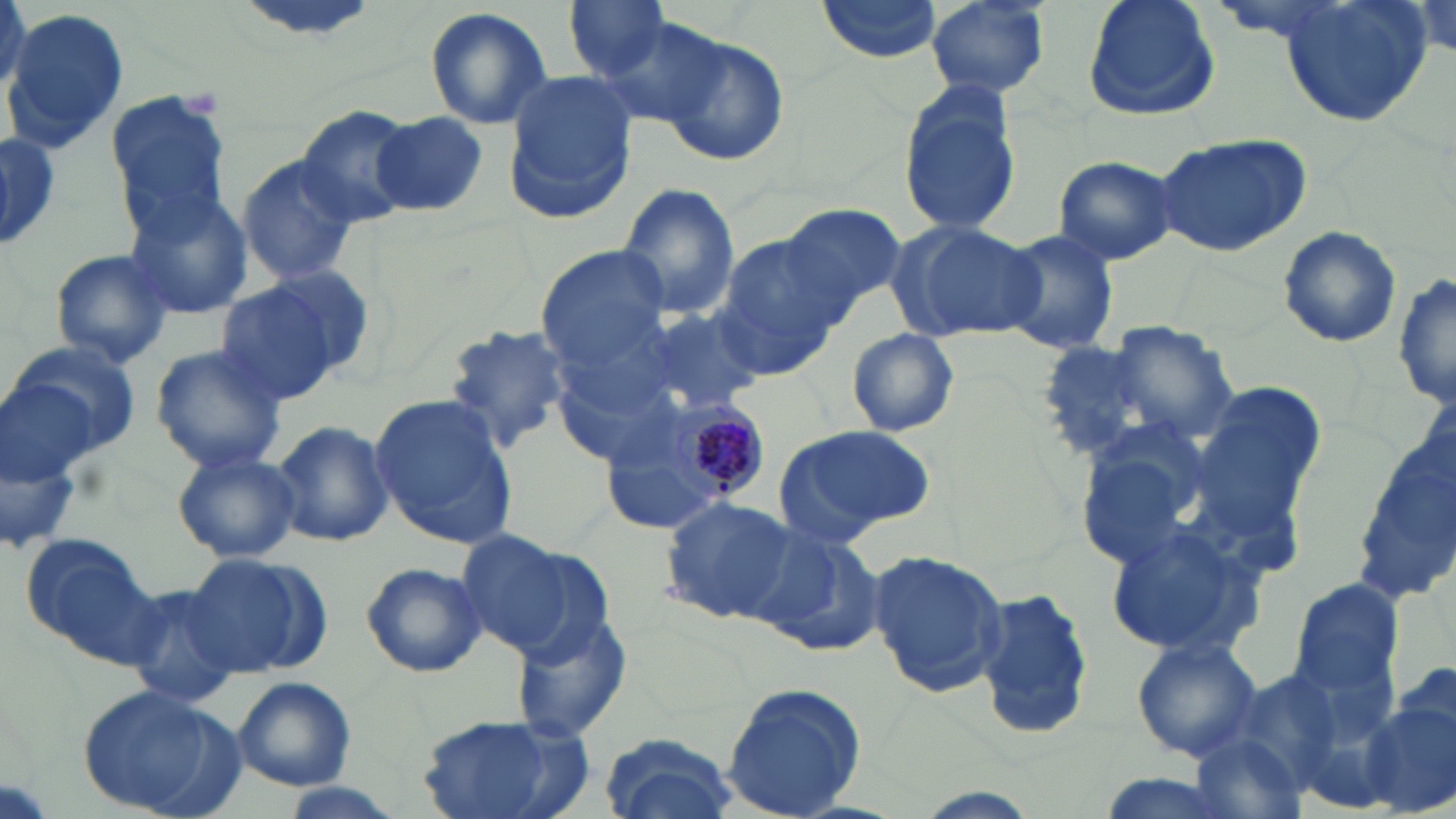

Approximate bounding boxes as named x1/y1/x2/y2 corners in pixels. Uninfected red blood cell locations: (x1=0, y1=0, x2=30, y2=98), (x1=815, y1=0, x2=950, y2=64), (x1=923, y1=0, x2=1052, y2=100), (x1=1083, y1=0, x2=1220, y2=123), (x1=1270, y1=0, x2=1434, y2=127), (x1=1411, y1=1, x2=1455, y2=54), (x1=564, y1=2, x2=674, y2=80), (x1=424, y1=6, x2=554, y2=132), (x1=3, y1=10, x2=128, y2=156), (x1=589, y1=17, x2=734, y2=128), (x1=654, y1=34, x2=787, y2=166), (x1=504, y1=73, x2=638, y2=221), (x1=898, y1=80, x2=1025, y2=239), (x1=104, y1=93, x2=234, y2=233), (x1=294, y1=105, x2=415, y2=223), (x1=375, y1=113, x2=488, y2=217), (x1=1154, y1=131, x2=1312, y2=258), (x1=0, y1=134, x2=61, y2=252), (x1=237, y1=154, x2=361, y2=286), (x1=1051, y1=155, x2=1179, y2=265), (x1=618, y1=184, x2=741, y2=322), (x1=120, y1=189, x2=255, y2=320), (x1=778, y1=203, x2=906, y2=313), (x1=889, y1=218, x2=1047, y2=343), (x1=1277, y1=224, x2=1404, y2=350), (x1=993, y1=229, x2=1123, y2=356), (x1=710, y1=236, x2=848, y2=379), (x1=539, y1=247, x2=669, y2=368), (x1=46, y1=248, x2=175, y2=369), (x1=260, y1=267, x2=379, y2=385), (x1=1394, y1=270, x2=1455, y2=412), (x1=214, y1=279, x2=348, y2=405), (x1=629, y1=307, x2=769, y2=420), (x1=441, y1=322, x2=578, y2=455), (x1=1103, y1=323, x2=1239, y2=445), (x1=846, y1=328, x2=960, y2=437), (x1=10, y1=338, x2=145, y2=461), (x1=1036, y1=342, x2=1170, y2=463), (x1=151, y1=345, x2=290, y2=473), (x1=1195, y1=382, x2=1327, y2=527), (x1=367, y1=393, x2=520, y2=547), (x1=1354, y1=412, x2=1455, y2=613), (x1=273, y1=418, x2=394, y2=547), (x1=774, y1=425, x2=935, y2=543), (x1=171, y1=450, x2=301, y2=564), (x1=658, y1=494, x2=799, y2=621), (x1=1100, y1=522, x2=1270, y2=662), (x1=746, y1=525, x2=884, y2=658), (x1=456, y1=528, x2=601, y2=657), (x1=20, y1=533, x2=163, y2=666), (x1=868, y1=550, x2=1011, y2=696), (x1=181, y1=552, x2=331, y2=678), (x1=360, y1=561, x2=488, y2=678), (x1=1286, y1=578, x2=1409, y2=708), (x1=120, y1=583, x2=245, y2=710), (x1=975, y1=584, x2=1092, y2=741), (x1=511, y1=609, x2=636, y2=744), (x1=1131, y1=636, x2=1263, y2=763), (x1=232, y1=676, x2=356, y2=790), (x1=720, y1=681, x2=867, y2=817), (x1=76, y1=684, x2=240, y2=819), (x1=1358, y1=686, x2=1456, y2=816), (x1=411, y1=715, x2=595, y2=819), (x1=597, y1=730, x2=736, y2=819), (x1=1188, y1=731, x2=1309, y2=819). Plasmodium malariae-infected red blood cell locations: (x1=663, y1=396, x2=769, y2=502). Platelet locations: (x1=178, y1=86, x2=223, y2=118). Slide-level diagnosis: Plasmodium malariae. Image is 1456×819 pixels. May-Grünwald-Giemsa stain. Thin blood film. Light microscopy. Single field of view. 1000x magnification.